Comment on the morphology of the erythrocytes.
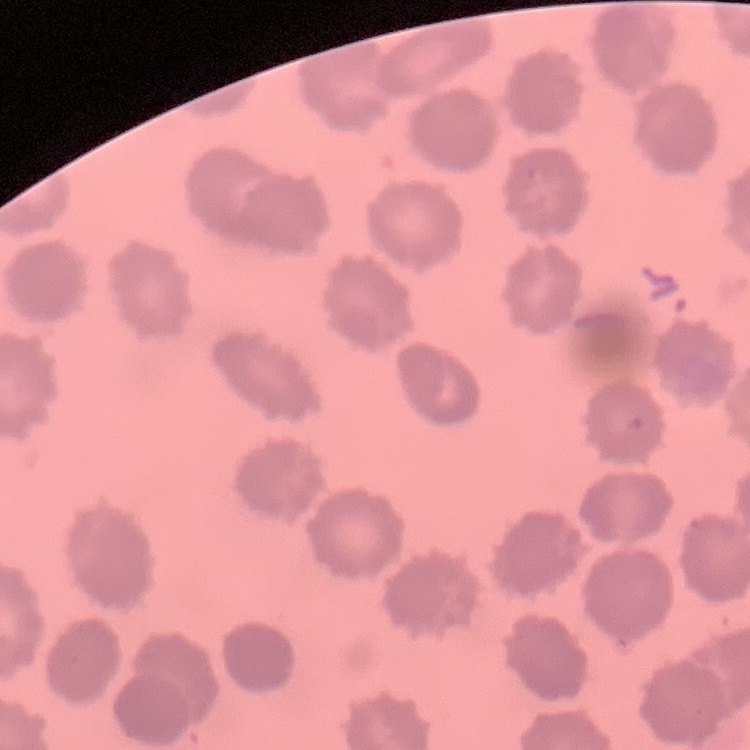
No rouleaux formation.

One tile cut from a larger photomicrograph. Stained with either Field's or Giemsa. Thin blood smear.